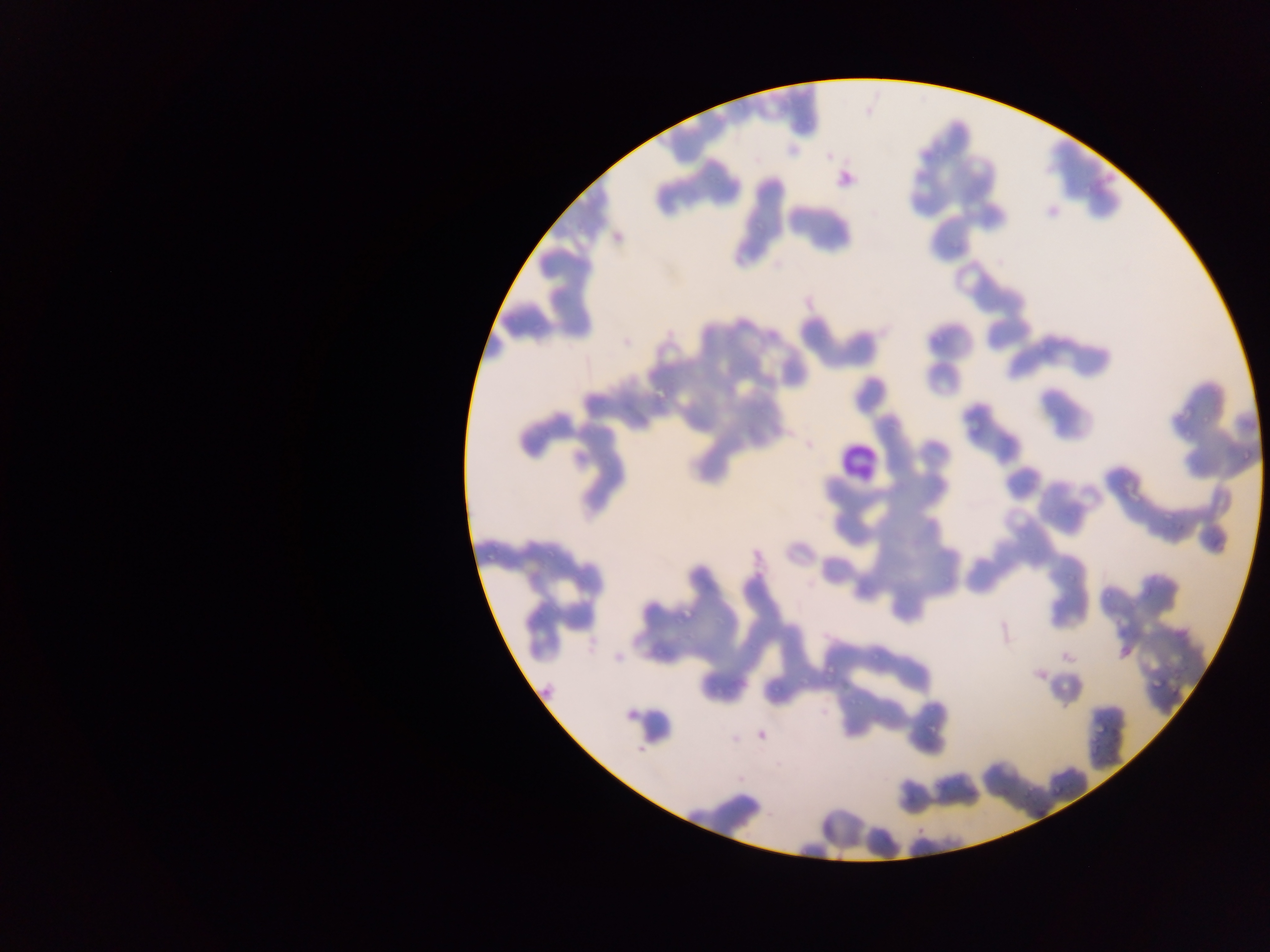

Approximate bounding boxes as left top right bottom in pixels.
Summary:
  - Malaria parasite locations: 931 327 952 350; 649 352 696 403; 1164 405 1200 424; 1238 454 1259 463; 1155 505 1177 519; 487 544 502 563; 676 600 709 624; 650 633 676 659; 825 662 832 679; 766 677 790 697; 713 678 731 706; 1146 682 1167 691; 911 712 948 740; 1086 717 1112 738; 1044 783 1069 800; 1012 791 1024 806
  - Leukocyte locations: 838 436 882 482
  - Capture: mobile-phone photograph through a microscope
  - Country: Ghana
  - Preparation: thin blood film
  - Field of view: single
  - Image size: 1270×952 pixels